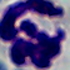
{
  "identification": "white blood cell",
  "modality": "micrograph",
  "magnification": "1000x"
}